State which parasite is depicted.
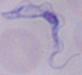
This is a trypanosome.

Captured at 1000x magnification. Micrograph.